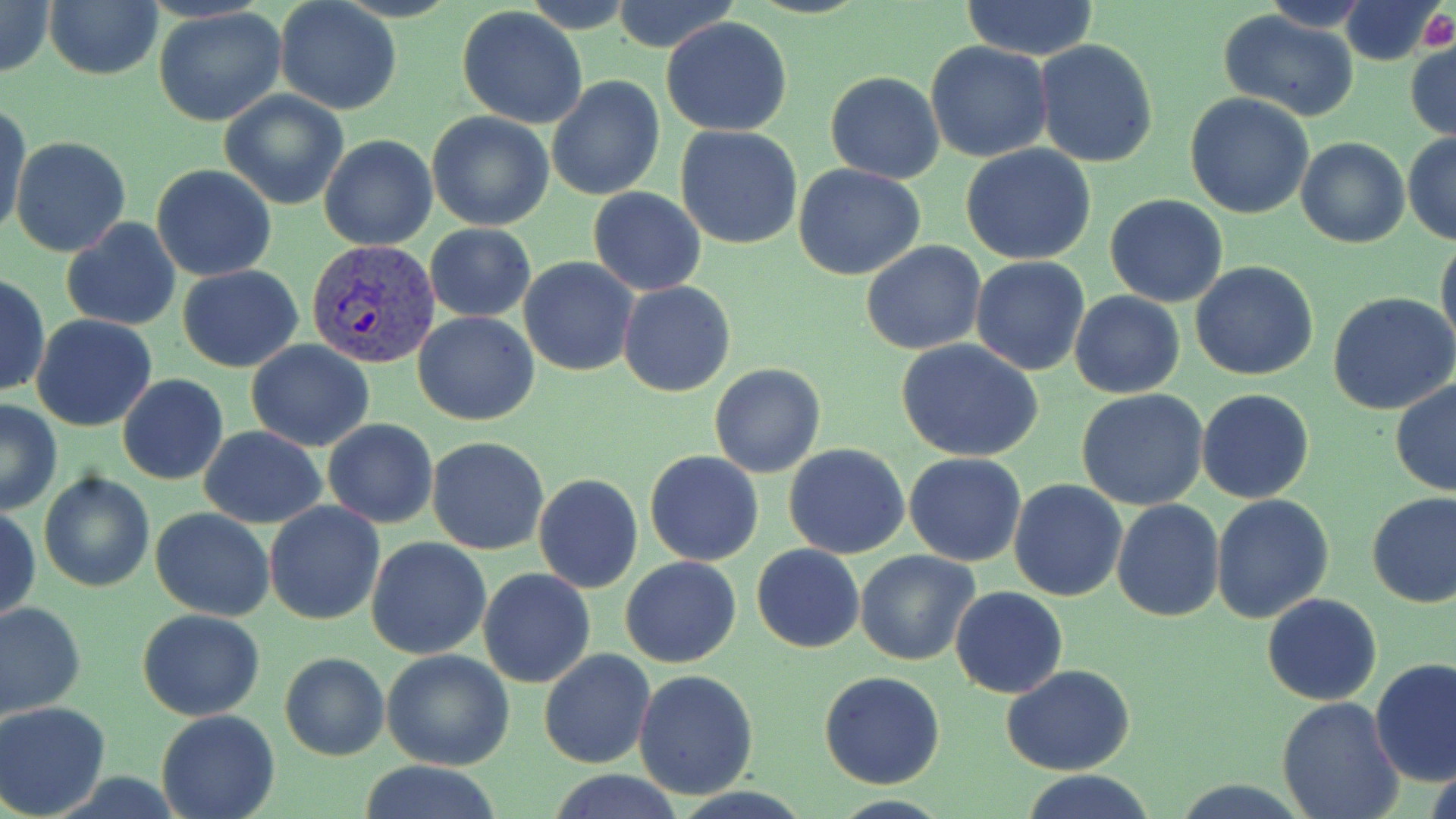
Approximate bounding boxes as (x1,y1)-(x2,y2) corner pairs in pixels. Plasmodium vivax-infected red blood cell locations: (307,239)-(441,369). Uninfected red blood cell locations: (0,0)-(54,80), (608,0)-(743,54), (960,0)-(1099,62), (45,1)-(161,81), (274,1)-(402,116), (1338,2)-(1444,66), (153,7)-(287,126), (458,7)-(589,130), (1220,11)-(1359,120), (661,16)-(793,136), (1035,40)-(1157,169), (1406,41)-(1455,142), (925,42)-(1053,165), (825,71)-(944,184), (547,75)-(666,202), (219,91)-(348,209), (1185,93)-(1314,219), (2,100)-(31,240), (427,111)-(554,232), (675,125)-(803,249), (1403,131)-(1456,245), (319,134)-(438,250), (10,136)-(131,257), (1296,138)-(1410,249), (960,145)-(1098,264), (794,163)-(926,280), (150,164)-(276,282), (588,187)-(706,295), (1105,194)-(1229,307), (61,217)-(182,332), (424,223)-(537,323), (1436,236)-(1456,350), (861,240)-(986,354), (970,256)-(1090,374), (519,257)-(638,375), (1190,262)-(1319,382), (177,265)-(304,374), (0,270)-(48,399), (617,281)-(736,397), (1069,291)-(1184,399), (1329,291)-(1456,413), (413,311)-(540,426), (30,313)-(157,432), (246,340)-(374,451), (898,341)-(1044,462), (710,364)-(825,478), (118,374)-(229,486), (1390,378)-(1456,495), (1196,388)-(1314,503), (1077,389)-(1209,511), (0,399)-(63,515), (323,418)-(438,529), (198,426)-(328,527), (426,436)-(550,555), (783,444)-(910,560), (645,450)-(763,567), (904,453)-(1028,567), (40,471)-(154,593), (534,474)-(642,592), (1008,480)-(1128,602), (1367,490)-(1456,608), (1210,494)-(1334,625), (1113,499)-(1225,621), (263,502)-(384,626), (1,505)-(40,624), (151,507)-(275,621), (366,537)-(490,659), (752,544)-(864,653), (856,550)-(980,665), (621,556)-(743,669), (478,567)-(596,688), (950,585)-(1069,698), (1262,593)-(1383,706), (0,600)-(85,719), (136,608)-(265,721), (538,649)-(655,768), (382,650)-(514,770), (278,652)-(390,762), (1370,659)-(1456,788), (1001,664)-(1135,776), (632,669)-(759,798), (819,671)-(945,788), (1276,697)-(1404,819), (0,701)-(115,819), (155,710)-(279,819), (353,761)-(509,818), (1017,770)-(1159,819). Platelet locations: (1420,11)-(1456,51). Slide-level diagnosis: Plasmodium vivax. Thin blood smear. One field of a larger specimen. Image is 1456×819 pixels. Captured at 1000x magnification. Optical microscopy. May-Grünwald-Giemsa-stained preparation.